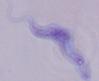

magnification = 1000x
modality = photomicrograph
identification = trypanosome